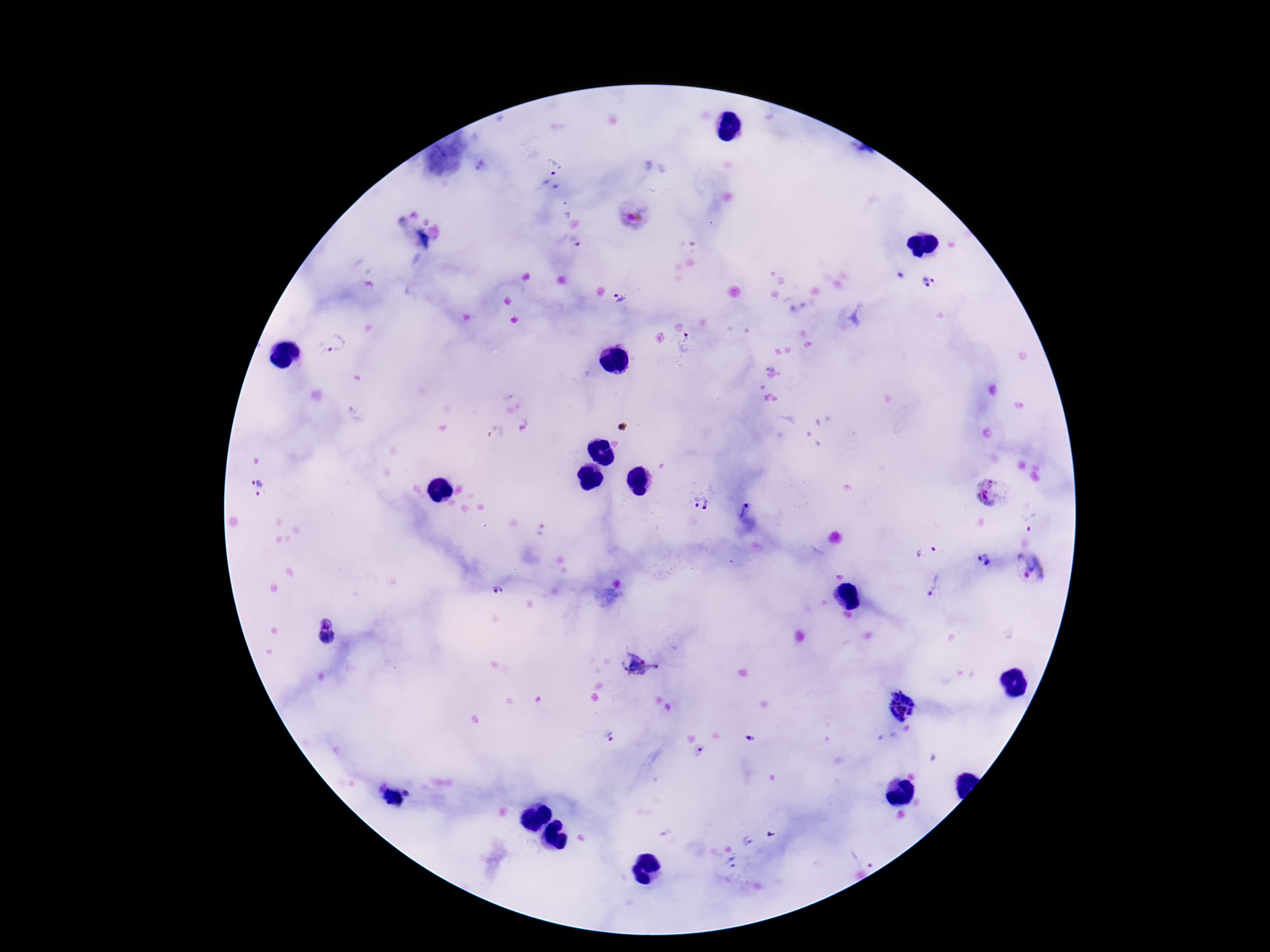 Approximate centers as {x, y} in pixels. Plasmodium parasite locations: {556, 162}, {634, 213}, {578, 244}, {928, 284}, {621, 298}, {689, 342}, {338, 343}, {260, 486}, {990, 491}, {702, 503}, {745, 509}, {1030, 519}, {926, 547}, {980, 560}, {1031, 567}, {935, 586}, {496, 591}, {326, 622}, {326, 638}, {642, 665}, {900, 705}, {608, 735}, {750, 739}, {698, 751}, {408, 792}, {748, 840}, {865, 856}. One field from this slide. Thick blood smear. Giemsa-stained preparation. Image is 1270×952 pixels. Patient malaria status: infected. Smartphone photograph taken through the microscope eyepiece. 100x magnification.